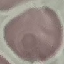 Result: no malaria parasites seen. Acquired by smartphone through the microscope eyepiece. Automatically extracted cell patch, resized to 64 × 64 pixels. Thin blood film. Giemsa stain.